Classify this cell by malaria status.
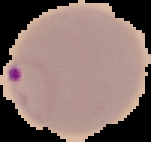

It is parasitized.

image size = 151×142 pixels
image type = segmented cell region with the area outside set to black
preparation = thin blood film